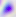

Micrograph. Captured at 400x magnification. Toxoplasma gondii is shown.